Assess the morphology of the erythrocytes.
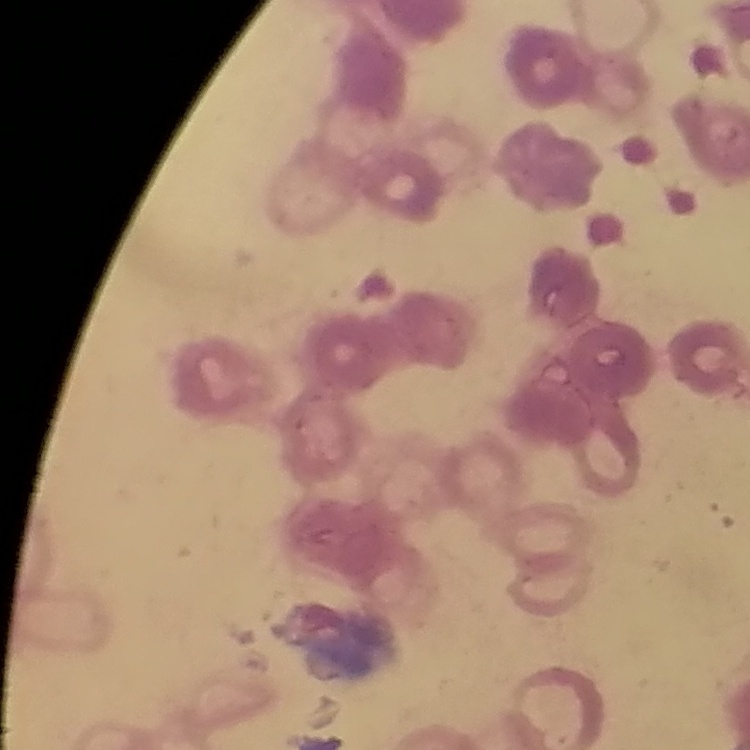

They show rouleaux formation.

Summary:
  - Stain: Field's or Giemsa
  - Image type: square crop of a larger photomicrograph
  - Preparation: thin blood film